Assess the morphology of the erythrocytes.
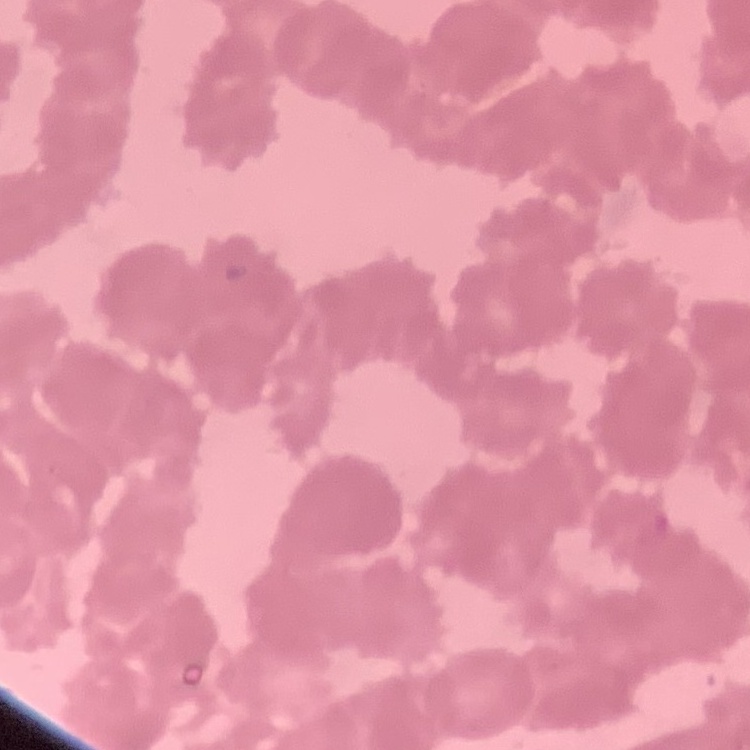
Rouleaux formation.

Summary:
  - Image type: square crop of a larger photomicrograph
  - Preparation: thin blood smear
  - Stain: Field's or Giemsa